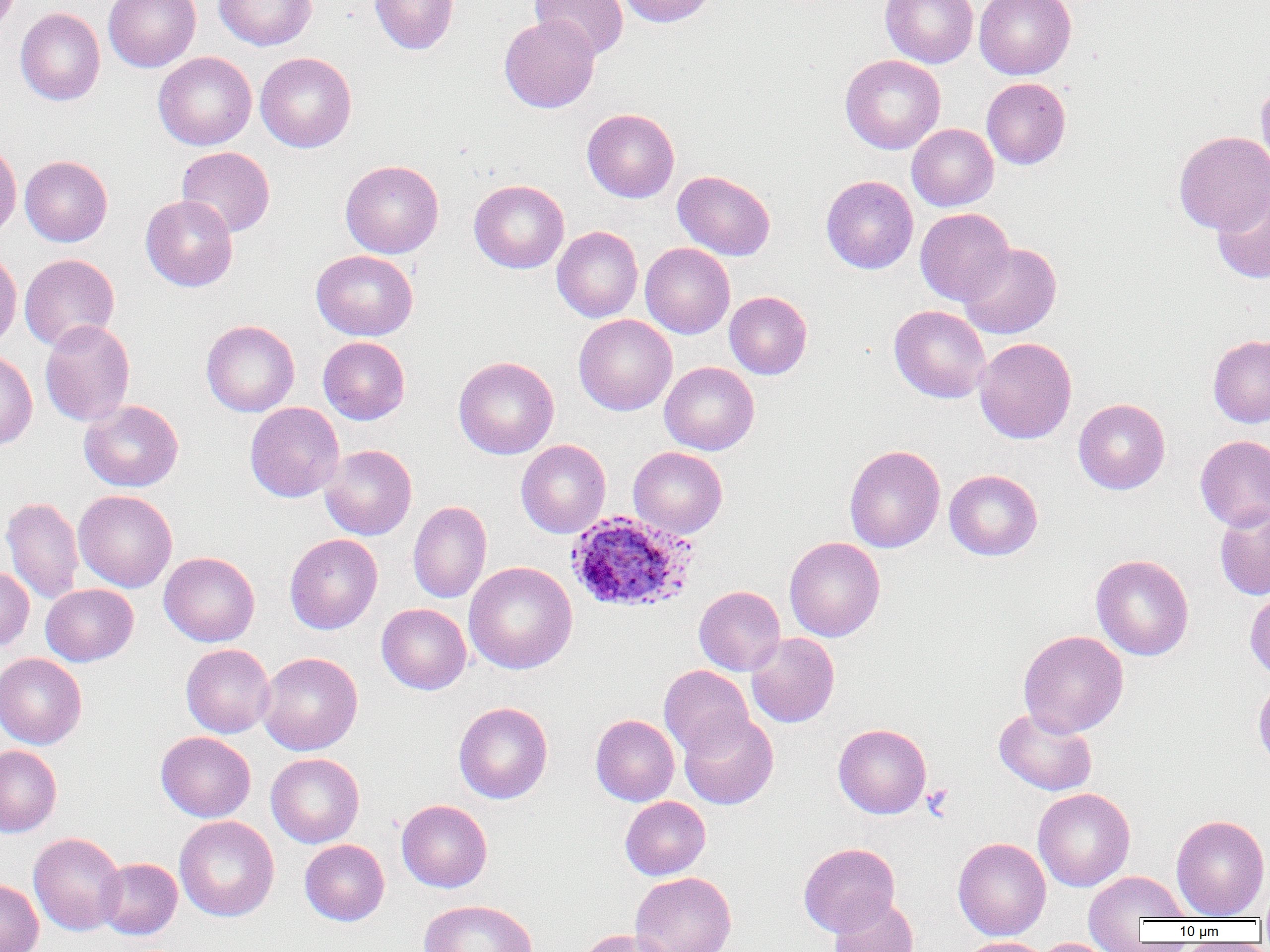 Approximate bounding boxes as (x1, y1, x2, y2) in pixels. Plasmodium ovale-infected red blood cell locations: (566, 511, 698, 614). Platelet locations: (922, 784, 954, 820). Uninfected red blood cell locations: (103, 0, 201, 72), (213, 0, 317, 50), (370, 0, 458, 54), (530, 0, 629, 60), (616, 0, 718, 27), (880, 0, 978, 68), (974, 0, 1076, 79), (15, 4, 200, 87), (15, 7, 105, 106), (499, 14, 600, 113), (153, 51, 256, 150), (255, 51, 357, 153), (840, 54, 946, 154), (981, 78, 1071, 169), (1256, 78, 1270, 174), (582, 108, 679, 202), (907, 123, 998, 211), (1173, 131, 1270, 235), (0, 140, 22, 244), (176, 146, 275, 238), (20, 155, 112, 247), (340, 160, 444, 258), (673, 170, 775, 261), (821, 175, 918, 274), (469, 179, 569, 273), (1211, 184, 1270, 284), (140, 195, 238, 292), (915, 208, 1014, 306), (552, 226, 643, 322), (958, 242, 1061, 339), (640, 243, 735, 338), (0, 249, 22, 352), (311, 250, 418, 341), (19, 254, 120, 351), (725, 291, 812, 379), (889, 305, 991, 403), (573, 314, 677, 415), (39, 320, 136, 427), (201, 320, 299, 417), (1208, 334, 1270, 427), (318, 336, 410, 424), (974, 337, 1077, 444), (0, 349, 37, 451), (453, 356, 559, 458), (660, 362, 759, 455), (1073, 398, 1170, 494), (79, 400, 184, 492), (245, 402, 344, 502), (1195, 435, 1270, 531), (516, 439, 611, 538), (320, 444, 417, 540), (844, 445, 945, 553), (628, 446, 727, 538), (944, 469, 1043, 560), (74, 490, 177, 592), (1, 496, 84, 604), (408, 500, 492, 603), (1214, 503, 1270, 601), (284, 533, 383, 634), (784, 536, 885, 641), (159, 551, 260, 647), (1090, 554, 1194, 660), (464, 561, 577, 674), (0, 565, 34, 651), (41, 583, 138, 666), (694, 585, 786, 675), (1245, 587, 1270, 683), (377, 603, 472, 694), (1018, 630, 1129, 737), (746, 633, 839, 728), (181, 644, 275, 738), (257, 651, 362, 755), (0, 653, 87, 749), (659, 665, 754, 757), (1252, 677, 1270, 773), (454, 701, 553, 804), (994, 707, 1097, 796), (679, 711, 778, 809), (590, 714, 679, 806), (833, 723, 932, 818), (155, 731, 256, 822), (0, 744, 62, 837), (266, 753, 364, 847), (1033, 788, 1135, 892), (620, 796, 710, 880), (396, 799, 492, 892), (1171, 814, 1269, 919), (174, 815, 279, 922), (28, 832, 127, 935), (952, 837, 1051, 941), (299, 839, 389, 926), (798, 842, 900, 936), (96, 858, 182, 939), (1083, 869, 1192, 945), (630, 872, 737, 952), (0, 878, 43, 952), (1258, 884, 1270, 928), (829, 896, 918, 952), (418, 899, 538, 952), (575, 928, 676, 952), (960, 937, 1051, 952), (1036, 938, 1117, 952). Slide-level diagnosis: Plasmodium ovale. Captured at 1000x magnification. Image is 1270×952 pixels. Single field of view. Thin blood film. Light microscopy.